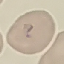

Malaria status: parasitized. Giemsa stain. Photographed with a smartphone camera at the microscope eyepiece. Cell patch, automatically extracted from a larger field of view and resized to 64 × 64 pixels. Thin blood film.